Assess for malaria.
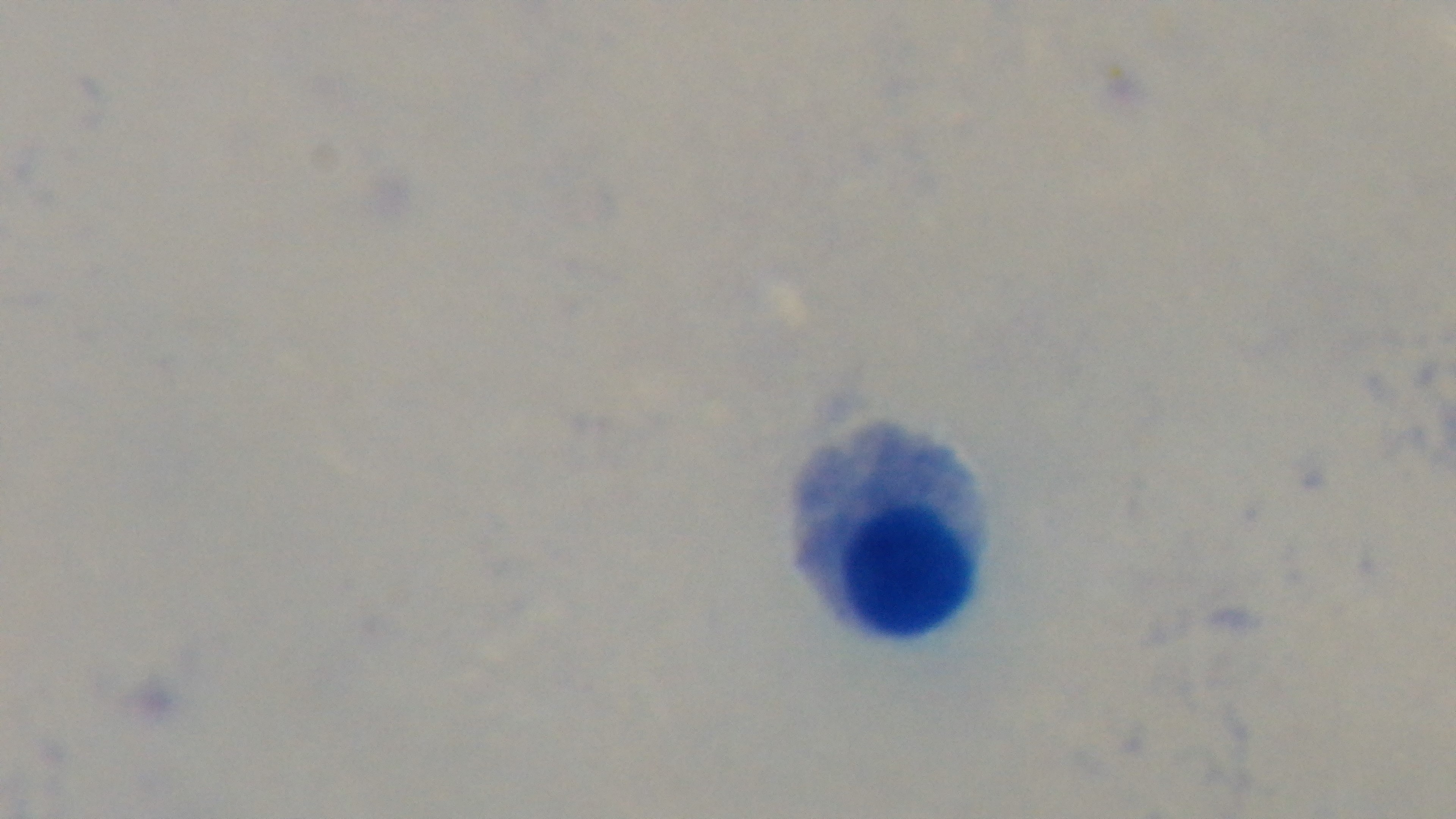
Negative.

preparation = thick smear
modality = light microscopy
capture = mounted 4K digital camera
objective = 100x oil immersion
stain = Giemsa
field of view = one from the slide